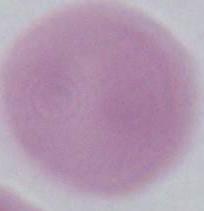
Summary:
  - Magnification: 1000x
  - Modality: photomicrograph
  - Identification: erythrocyte